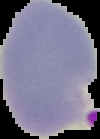 Image is 100×139 pixels. From a thin blood smear. The area outside the segmented cell region is set to black. Malaria status: parasitized.